Assess the morphology of the erythrocytes.
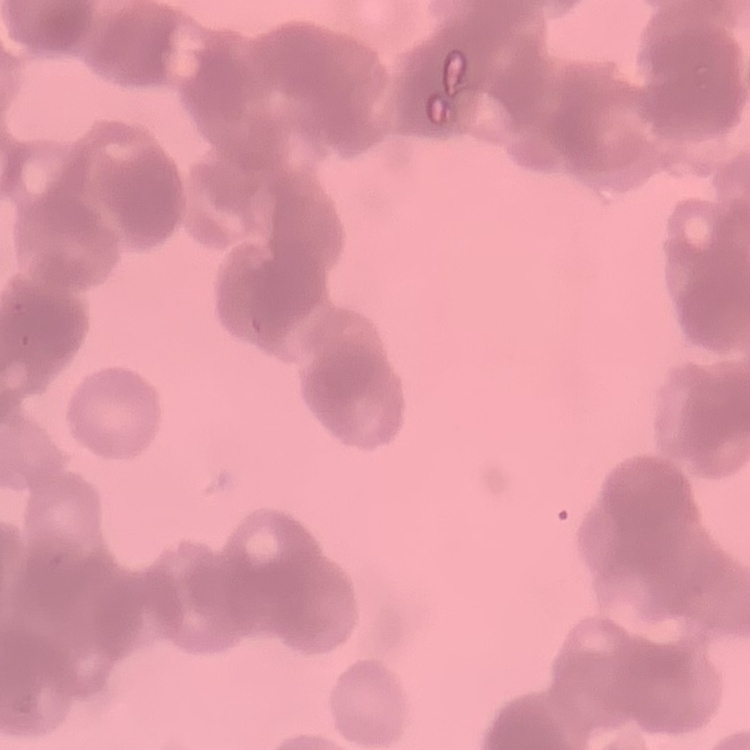

They show rouleaux formation.

One tile cut from a larger photomicrograph. Thin peripheral smear. Stained with either Field's or Giemsa.